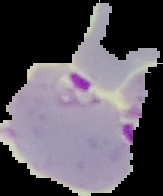

Summary:
  - Malaria status: parasitized
  - Image size: 163×196 pixels
  - Preparation: thin blood film
  - Image type: segmented cell region with the area outside set to black